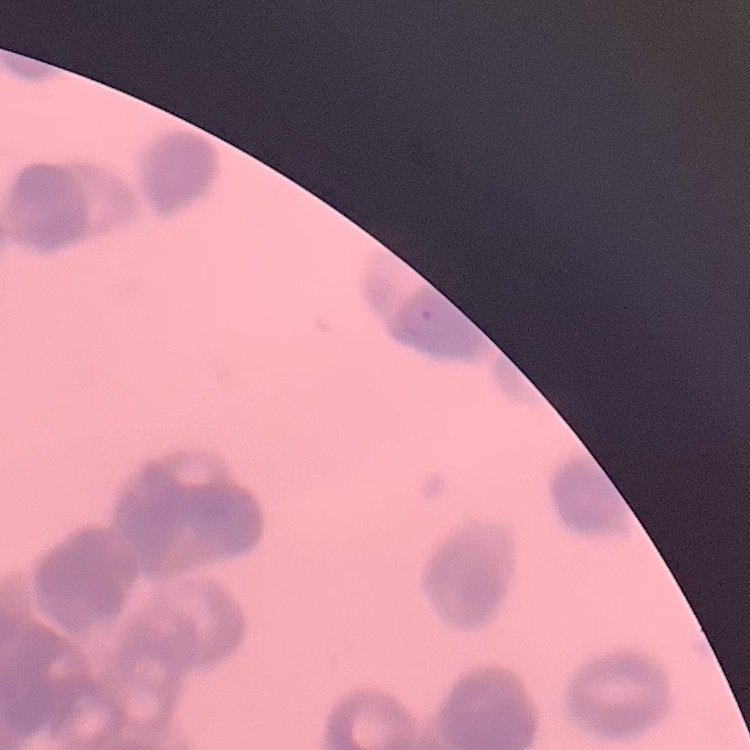
{
  "erythrocyte_morphology": "rouleaux formation",
  "image_type": "square crop of a larger photomicrograph",
  "stain": "Field's or Giemsa",
  "preparation": "thin peripheral smear"
}